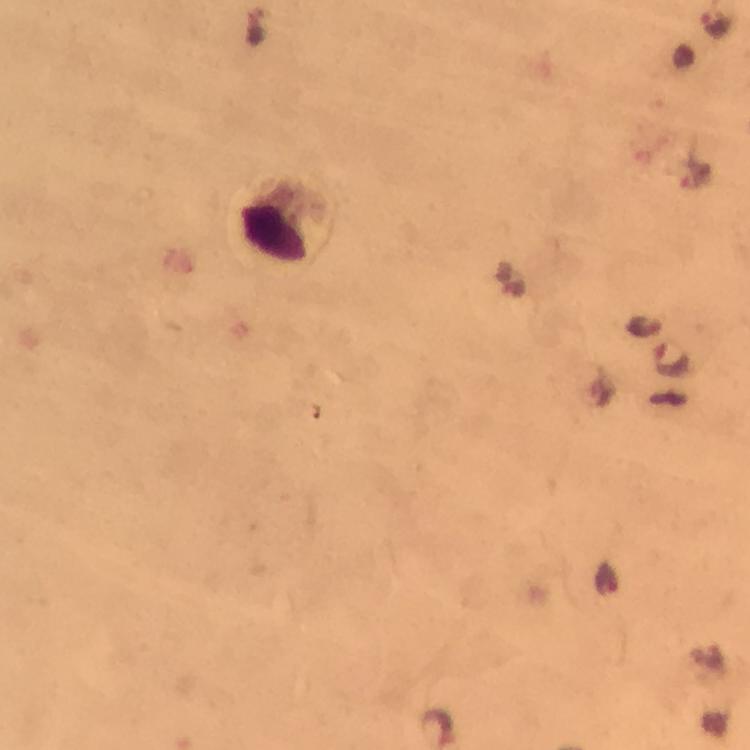

{
  "capture": "smartphone mounted on the microscope",
  "cropped_from": "one field of view",
  "malaria_parasite_locations": "approximate centers as (x, y) in pixels: (673, 359)",
  "context": "from a diagnostic examination for malaria",
  "image_size": "750×750 pixels",
  "leukocyte_locations": "approximate centers as (x, y) in pixels: (282, 225)",
  "stain": "Giemsa",
  "preparation": "thick blood film",
  "magnification": "100x",
  "immersion_oil": "used"
}